Point out each Plasmodium parasite.
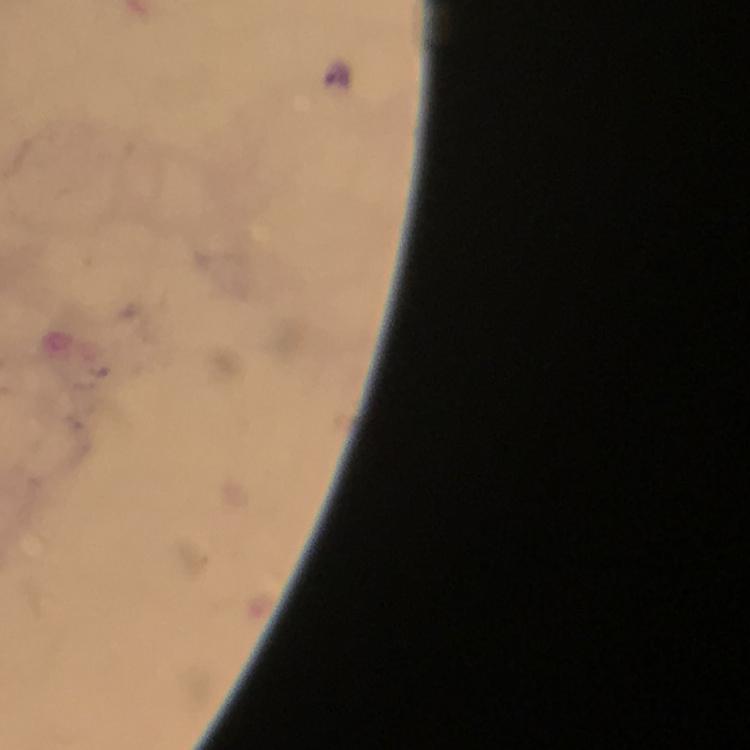
Approximate centers as (x, y) in pixels.
Plasmodium parasites: (336, 71).

Summary:
  - Context: from a diagnostic examination for malaria
  - Image size: 750×750 pixels
  - Stain: Giemsa
  - Cropped from: a single field of view
  - Magnification: 100x
  - Immersion oil: used
  - Capture: smartphone mounted on the microscope
  - Preparation: thick smear